Describe the morphology of the erythrocytes.
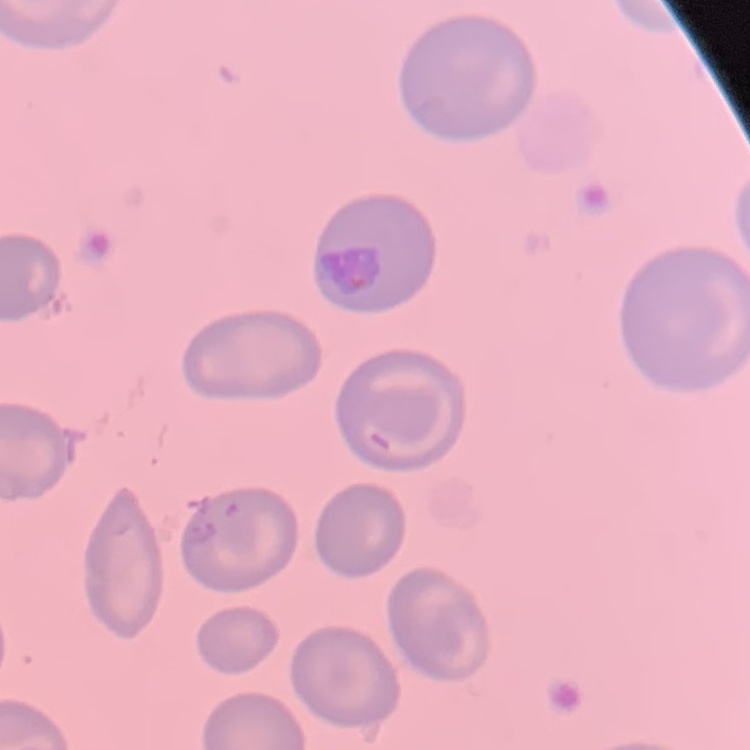
They show no rouleaux formation.

{
  "image_type": "square crop of a larger photomicrograph",
  "preparation": "thin blood smear",
  "stain": "Field's or Giemsa"
}